Locate malaria parasites and leukocytes.
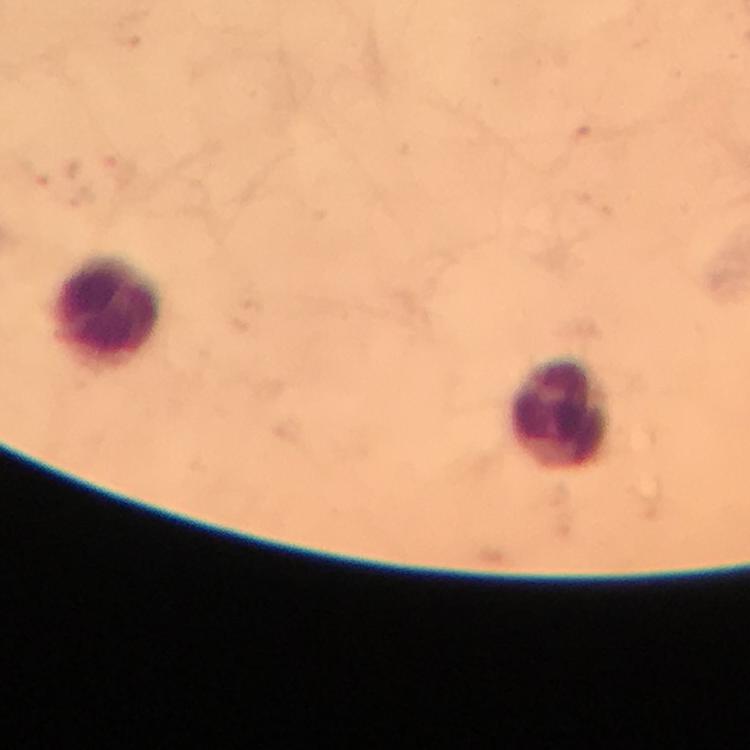

No malaria parasites detected.
Approximate object centers, in pixels from the top-left corner.
Leukocytes: (x=109, y=312), (x=563, y=416).

cropped from = one field of view
stain = Giemsa
image size = 750×750 pixels
immersion oil = applied
preparation = thick blood film
magnification = 100x
context = from a diagnostic examination for malaria
capture = smartphone mounted on the microscope